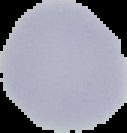
Summary:
  - Malaria status: uninfected
  - Image type: cell region segmented out of the field of view; surrounding area masked to black
  - Preparation: thin blood film
  - Image size: 127×133 pixels